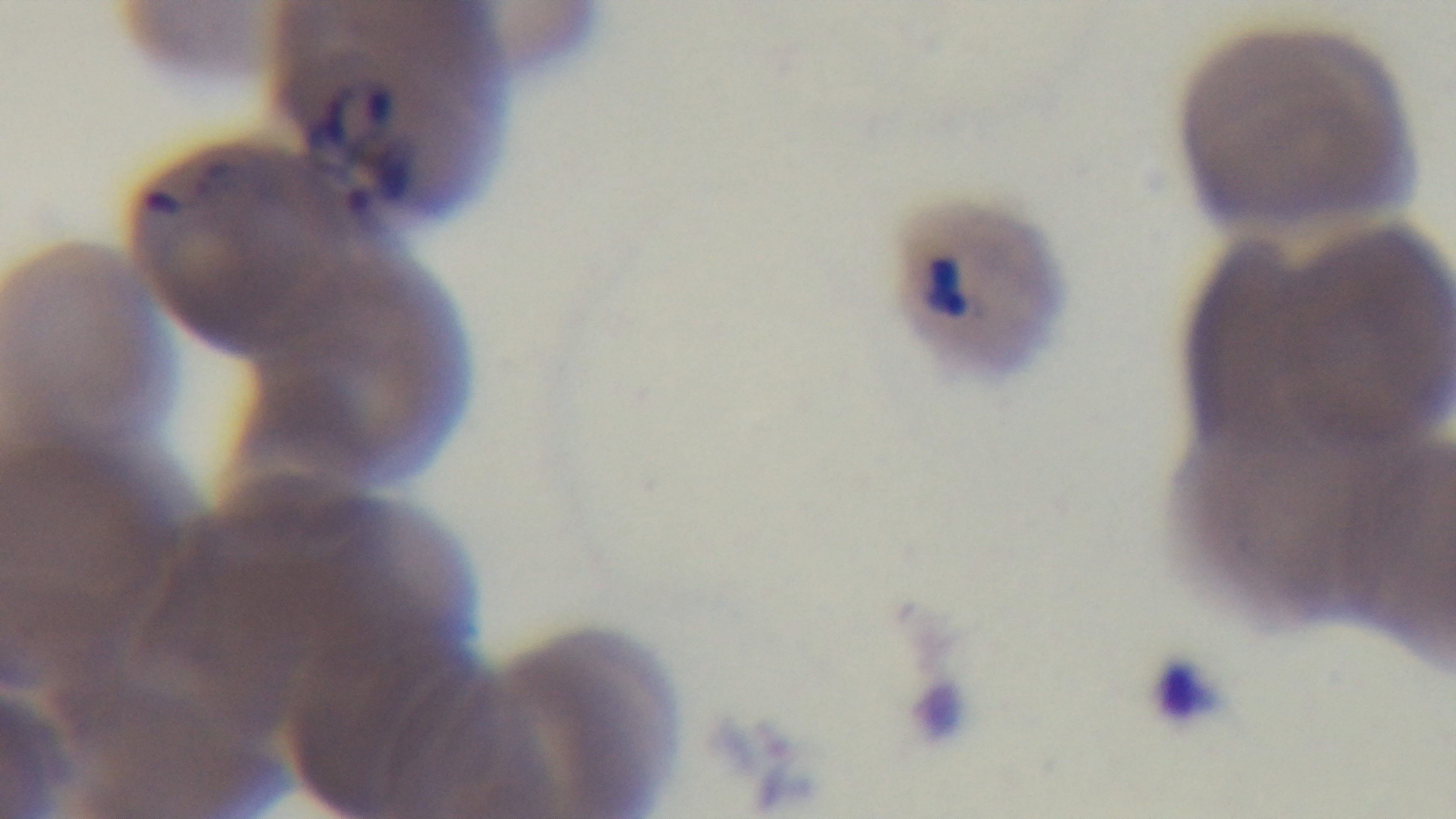

Summary:
  - Preparation: thin blood film
  - Modality: light microscopy
  - Objective: 100x oil immersion
  - Malaria status: positive
  - Capture: mounted 4K digital camera
  - Stain: Giemsa
  - Field of view: single